Classify this cell by malaria status.
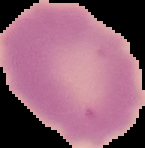
Uninfected.

image type = segmented cell region with the area outside set to black
preparation = thin blood film
image size = 145×148 pixels